Comment on the morphology of the erythrocytes.
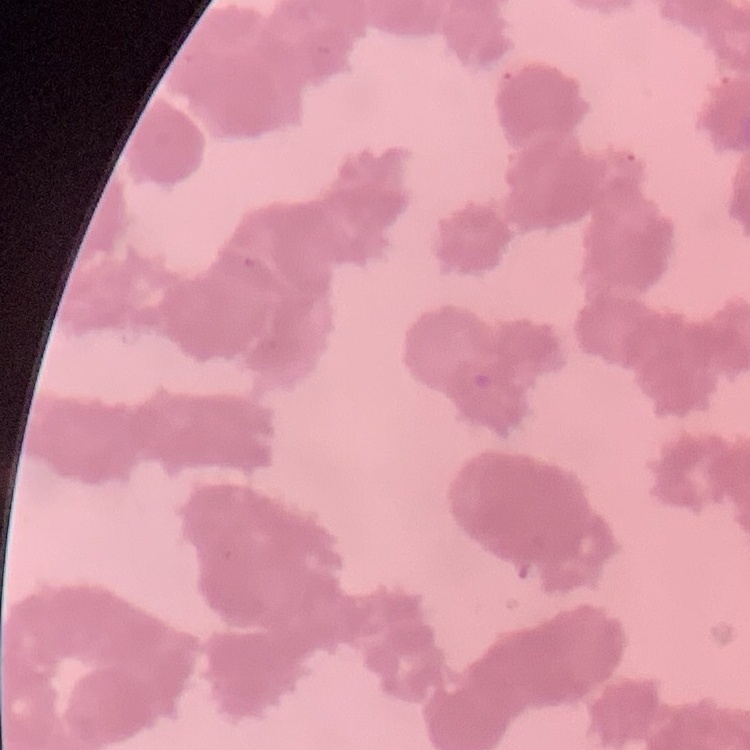

Rouleaux formation.

Field's or Giemsa stain. Thin peripheral smear. One tile cut from a larger photomicrograph.